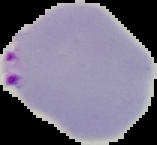

malaria_status: parasitized
preparation: thin blood film
image_type: segmented cell region on a black background
image_size: 157×145 pixels